Point out each Plasmodium parasite.
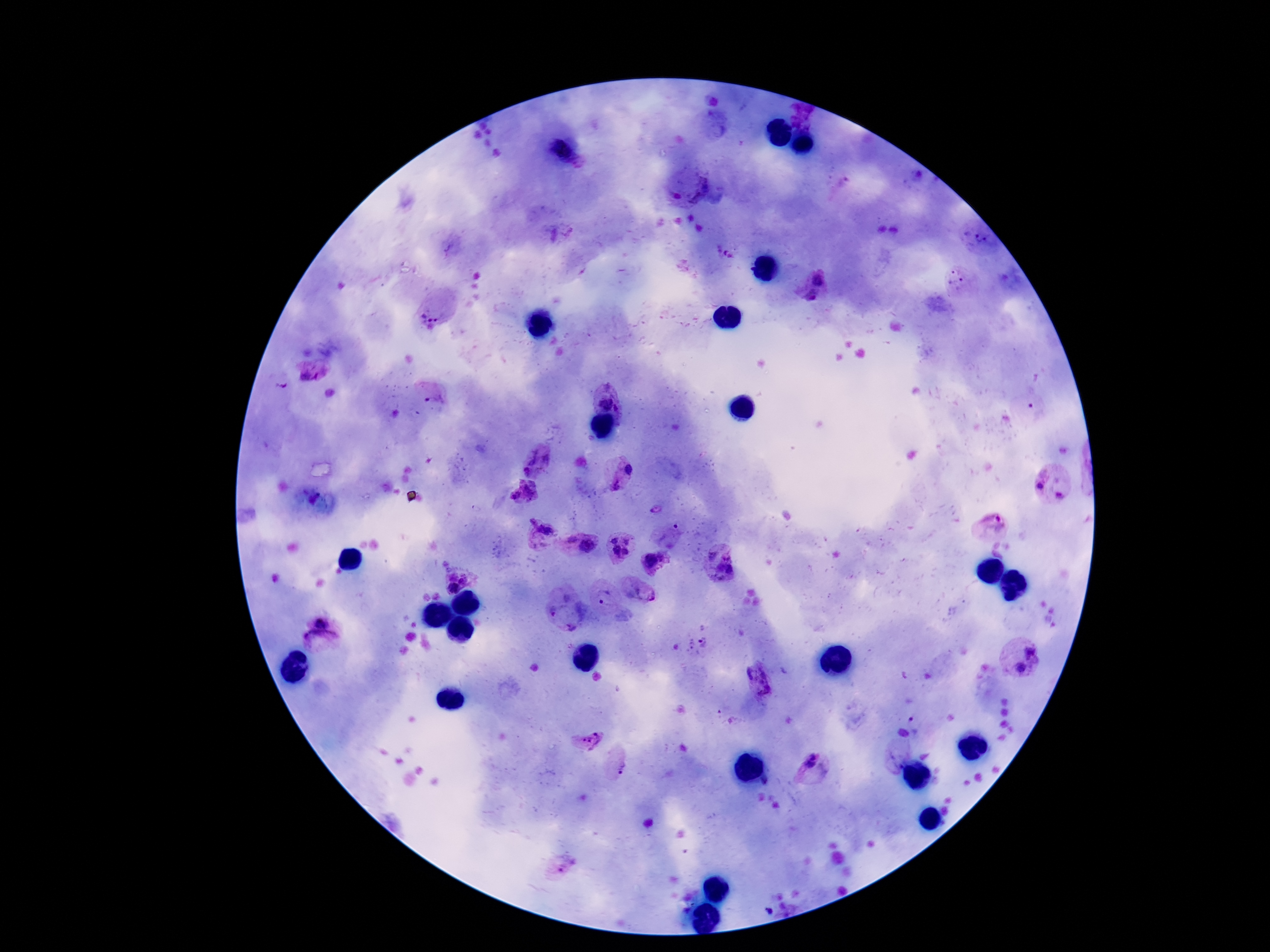
Approximate object centers, in pixels from the top-left corner.
Plasmodium parasites: (x=562, y=150), (x=690, y=187), (x=980, y=235), (x=728, y=255), (x=818, y=275), (x=957, y=281), (x=810, y=296), (x=432, y=316), (x=314, y=372), (x=612, y=397), (x=437, y=401), (x=526, y=453), (x=548, y=458), (x=628, y=469), (x=528, y=472), (x=1039, y=483), (x=532, y=484), (x=617, y=487), (x=528, y=493), (x=1059, y=494), (x=513, y=496), (x=533, y=523), (x=991, y=523), (x=548, y=530), (x=614, y=538), (x=572, y=540), (x=627, y=540), (x=587, y=545), (x=616, y=551), (x=626, y=552), (x=710, y=554), (x=727, y=556), (x=651, y=560), (x=727, y=571), (x=466, y=577), (x=453, y=587), (x=646, y=591), (x=604, y=598), (x=556, y=609), (x=320, y=621), (x=572, y=624), (x=321, y=639), (x=1032, y=651), (x=1019, y=669), (x=759, y=676), (x=589, y=737), (x=895, y=759), (x=810, y=760), (x=621, y=766), (x=567, y=864), (x=768, y=911).

Summary:
  - Stain: Giemsa
  - Patient malaria status: positive
  - Image size: 1270×952 pixels
  - Preparation: thick blood smear
  - Magnification: 100x
  - Capture: smartphone camera through the microscope eyepiece
  - Field of view: single